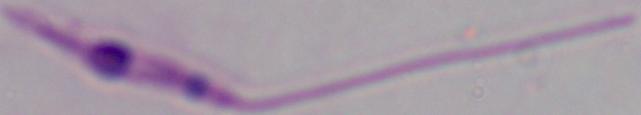
A Leishmania parasite is seen. 1000x magnification. Micrograph.